Classify this cell by malaria status.
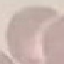

Uninfected.

Thin blood film. Giemsa-stained preparation. Photographed with a smartphone camera at the microscope eyepiece. Cell patch, automatically extracted from a larger field of view and resized to 64 × 64 pixels.